Locate every Plasmodium parasite.
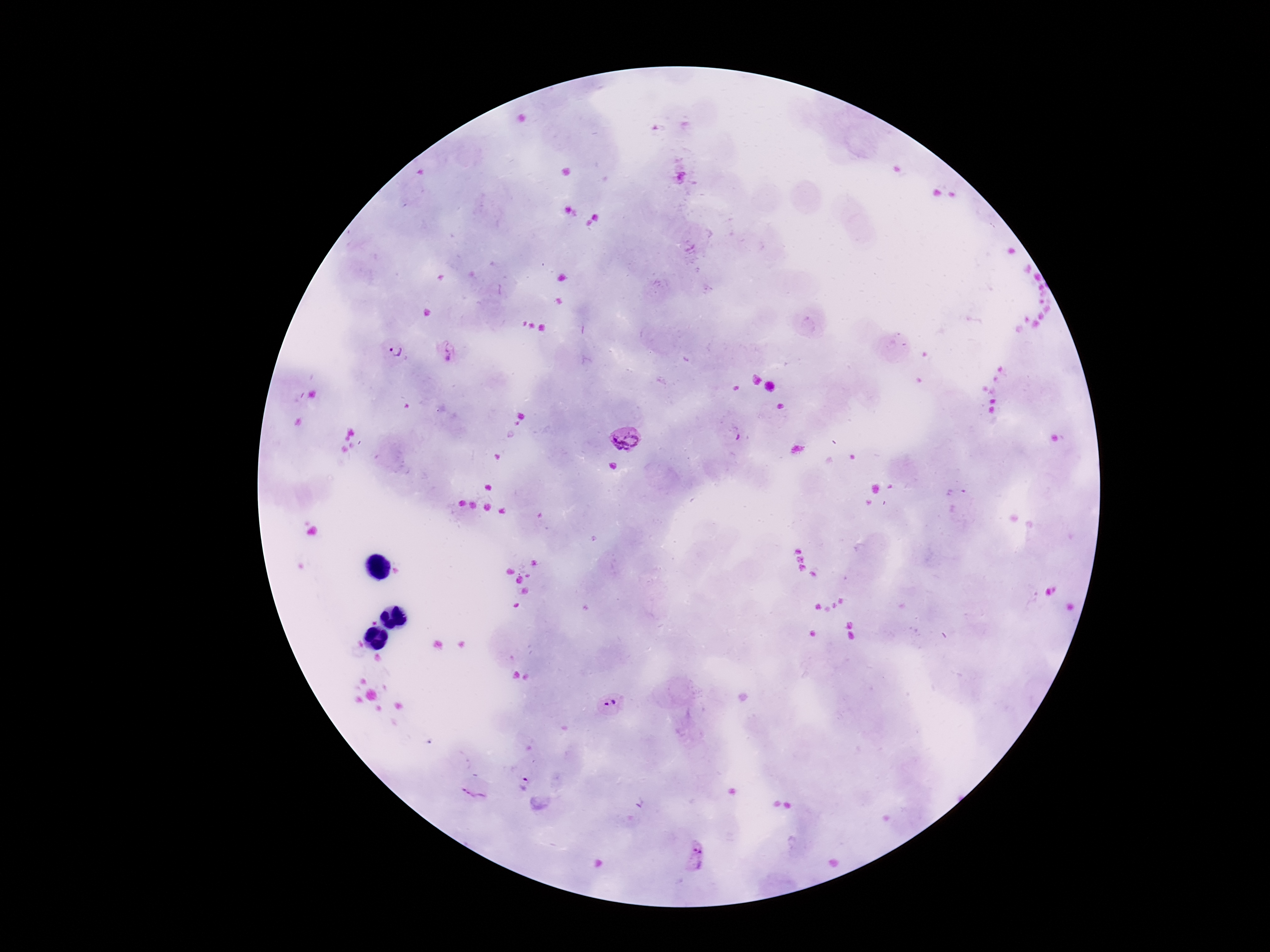
Approximate centers as {x, y} in pixels.
Plasmodium parasites: {447, 352}, {397, 353}, {738, 434}, {623, 440}, {611, 703}, {524, 783}, {476, 790}, {697, 855}.

Summary:
  - Field of view: one from this slide
  - Capture: smartphone camera through the microscope eyepiece
  - Stain: Giemsa
  - Preparation: thick blood film
  - Patient malaria status: infected
  - Magnification: 100x
  - Image size: 1270×952 pixels